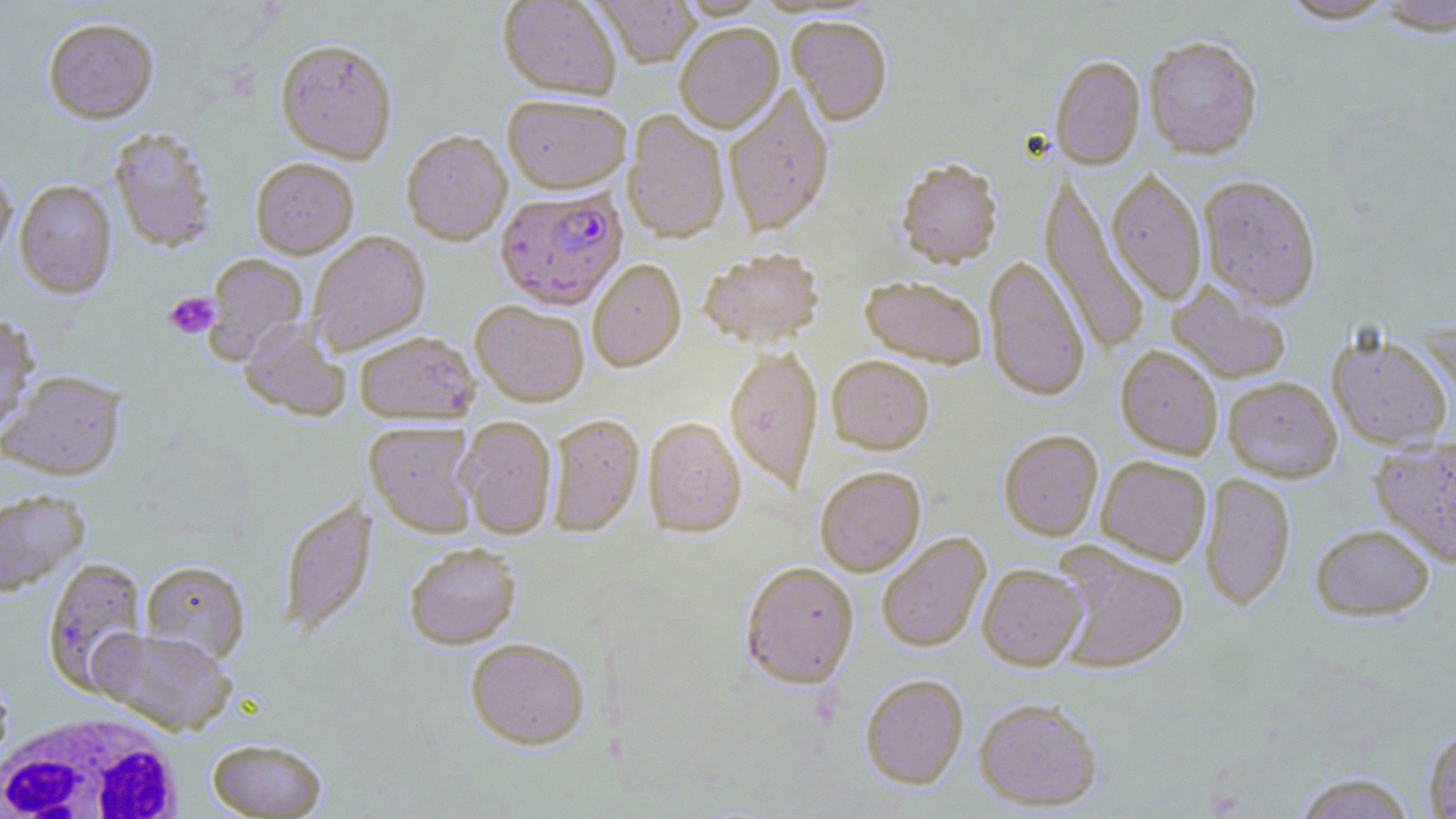
Approximate bounding boxes as (x1,y1)-(x2,y2) corner pairs in pixels. White blood cell locations: (2,709)-(188,819). Plasmodium falciparum-infected red blood cell locations: (495,188)-(628,310). Uninfected red blood cell locations: (497,0)-(620,101), (591,0)-(700,70), (675,0)-(771,21), (1278,0)-(1399,26), (1375,0)-(1456,39), (43,16)-(159,124), (787,18)-(892,129), (675,25)-(784,135), (1144,38)-(1263,160), (276,40)-(397,164), (1050,57)-(1145,171), (723,87)-(835,238), (503,97)-(631,196), (623,111)-(729,244), (107,127)-(218,253), (401,131)-(512,246), (250,158)-(359,259), (0,161)-(17,268), (895,161)-(1004,272), (1106,170)-(1207,306), (1038,173)-(1151,356), (1198,175)-(1322,311), (15,180)-(117,298), (308,231)-(430,354), (699,250)-(824,348), (203,253)-(308,362), (983,256)-(1090,404), (588,259)-(686,373), (859,277)-(987,369), (1167,282)-(1291,384), (470,301)-(589,407), (0,312)-(39,439), (239,320)-(351,421), (354,331)-(480,424), (1327,332)-(1453,451), (1115,346)-(1223,460), (724,347)-(823,494), (827,357)-(934,455), (1,369)-(126,479), (1223,377)-(1342,482), (546,414)-(644,536), (457,416)-(557,539), (643,418)-(746,538), (365,422)-(479,538), (999,430)-(1104,542), (1369,435)-(1456,568), (1096,456)-(1211,566), (814,467)-(926,577), (1199,473)-(1296,611), (0,489)-(89,595), (278,497)-(376,635), (1310,524)-(1434,621), (877,532)-(992,653), (404,543)-(521,649), (1052,546)-(1190,675), (42,556)-(150,693), (140,559)-(251,664), (740,562)-(859,689), (978,564)-(1087,671), (88,627)-(236,735), (465,638)-(590,749), (0,661)-(14,772), (860,673)-(969,789), (855,681)-(1098,791), (973,698)-(1104,812), (1422,727)-(1456,818), (206,737)-(328,817), (1293,772)-(1417,818). Platelet locations: (163,292)-(219,339). Slide-level diagnosis: Plasmodium falciparum. May-Grünwald-Giemsa-stained preparation. Image is 1456×819 pixels. 1000x magnification. Optical microscopy. Thin blood smear. Single field of view.